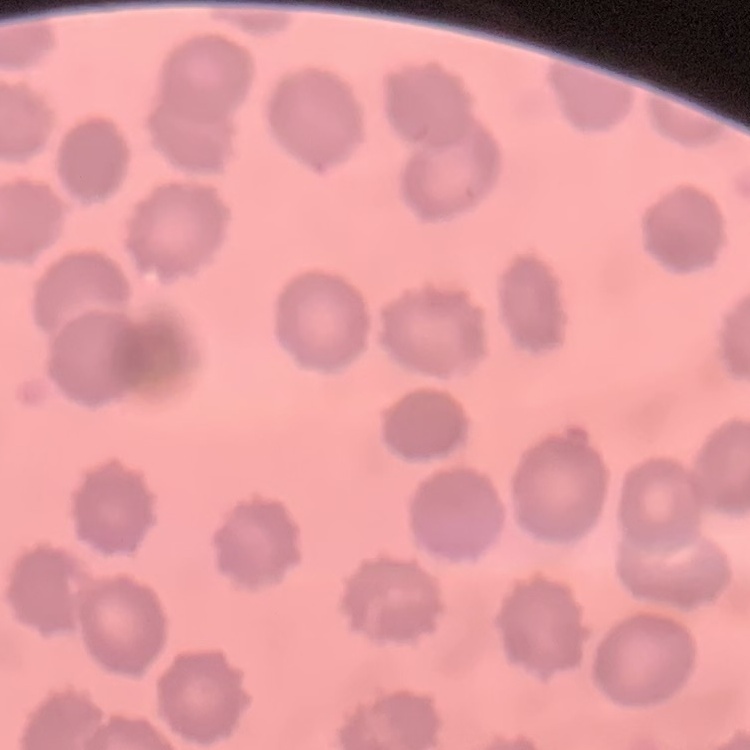

{
  "red_blood_cell_morphology": "no rouleaux formation",
  "preparation": "thin blood smear",
  "stain": "Field's or Giemsa",
  "image_type": "one tile cut from a larger photomicrograph"
}